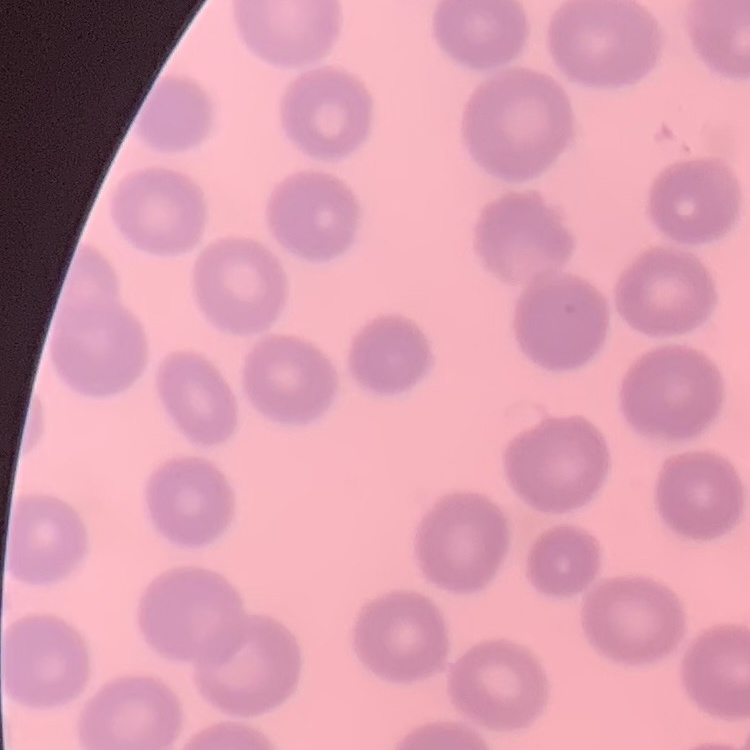

erythrocyte_morphology: no rouleaux formation
preparation: thin blood smear
stain: Field's or Giemsa
image_type: square crop of a larger photomicrograph